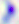

Photomicrograph. 400x magnification. Toxoplasma gondii is shown.